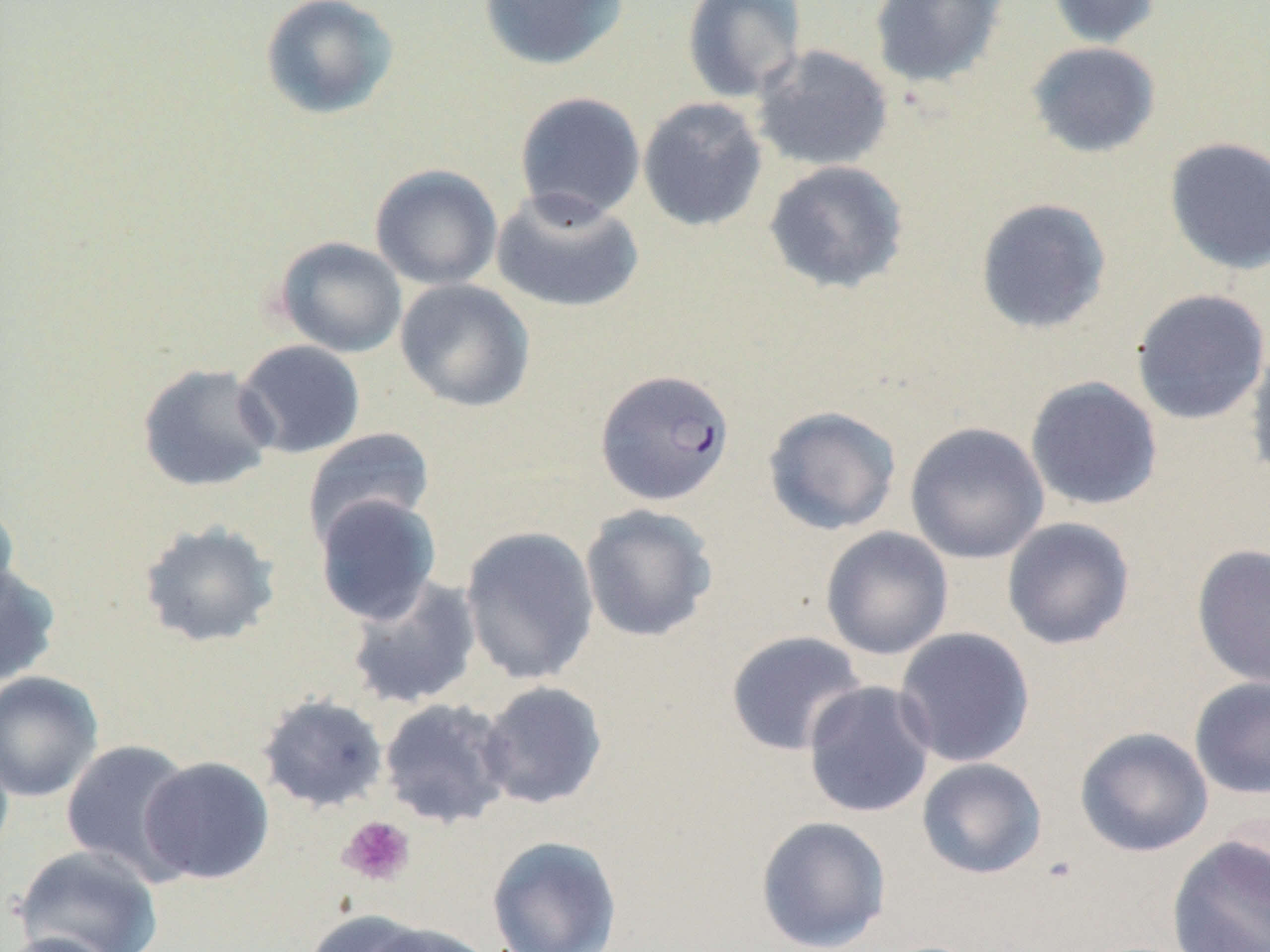
slide-level diagnosis = Plasmodium falciparum
preparation = thin blood film
field of view = one of a larger specimen
magnification = 1000x
stain = May-Grünwald-Giemsa
Plasmodium falciparum-infected red blood cell locations = approximate bounding boxes as (x1,y1)-(x2,y2) corner pairs in pixels: (594,369)-(735,506)
uninfected red blood cell locations = approximate bounding boxes as (x1,y1)-(x2,y2) corner pairs in pixels: (260,0)-(399,121), (477,0)-(629,71), (681,0)-(807,103), (868,0)-(1008,88), (1045,0)-(1164,49), (1026,41)-(1162,159), (750,44)-(895,172), (514,91)-(646,222), (637,97)-(768,232), (1164,136)-(1270,275), (763,159)-(909,295), (370,164)-(503,290), (491,188)-(644,314), (975,197)-(1112,335), (274,237)-(408,358), (395,278)-(535,413), (1130,288)-(1270,425), (1245,334)-(1270,488), (234,340)-(366,459), (136,362)-(279,493), (1024,375)-(1164,511), (762,406)-(902,536), (904,421)-(1049,565), (303,427)-(435,546), (314,494)-(442,626), (0,501)-(21,618), (579,503)-(718,643), (1001,517)-(1136,650), (136,520)-(282,649), (460,525)-(600,686), (820,526)-(954,660), (1191,544)-(1270,690), (0,563)-(61,687), (345,575)-(483,710), (893,627)-(1035,768), (725,630)-(867,757), (0,671)-(104,802), (1189,676)-(1270,800), (802,680)-(937,819), (477,681)-(608,810), (256,693)-(389,814), (378,698)-(515,829), (1075,726)-(1214,858), (60,739)-(199,883), (138,756)-(275,885), (916,757)-(1047,879), (755,815)-(891,951), (486,835)-(623,952), (1166,835)-(1270,952), (11,844)-(164,952), (302,908)-(436,952), (360,921)-(497,952), (0,931)-(124,952)
platelet locations = approximate bounding boxes as (x1,y1)-(x2,y2) corner pairs in pixels: (338,816)-(415,886)
modality = optical microscopy
image size = 1270×952 pixels